State which parasite is depicted.
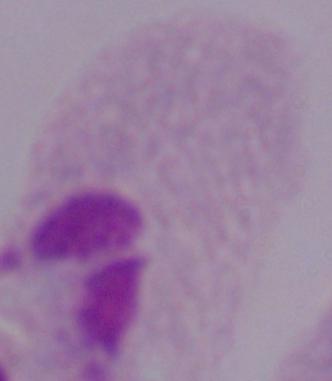

This is a trichomonad.

magnification: 1000x
modality: photomicrograph